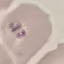

Result: malaria parasites detected. Automatically extracted cell patch, resized to 64 × 64 pixels. Acquired by smartphone through the microscope eyepiece. Giemsa stain. Thin smear of blood.